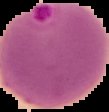

Summary:
  - Preparation: thin blood film
  - Result: malaria parasites detected
  - Image type: segmented cell region with the area outside set to black
  - Image size: 109×112 pixels